Name the parasite shown.
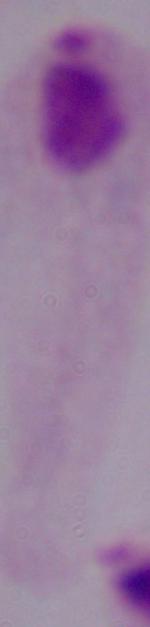

A trichomonad.

{
  "magnification": "1000x",
  "modality": "photomicrograph"
}